Describe the morphology of the red blood cells.
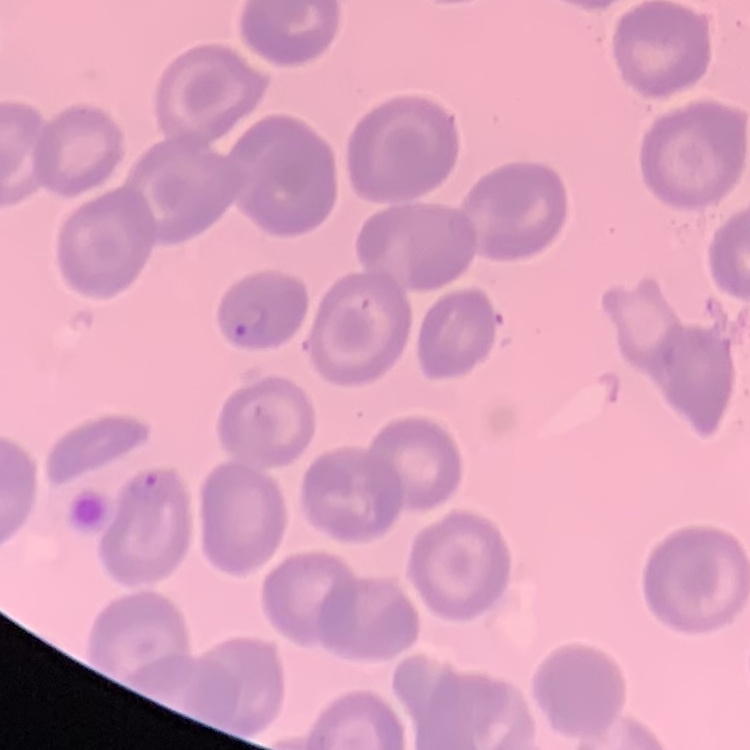
No rouleaux formation.

stain = Field's or Giemsa
image type = square crop of a larger photomicrograph
preparation = thin peripheral smear